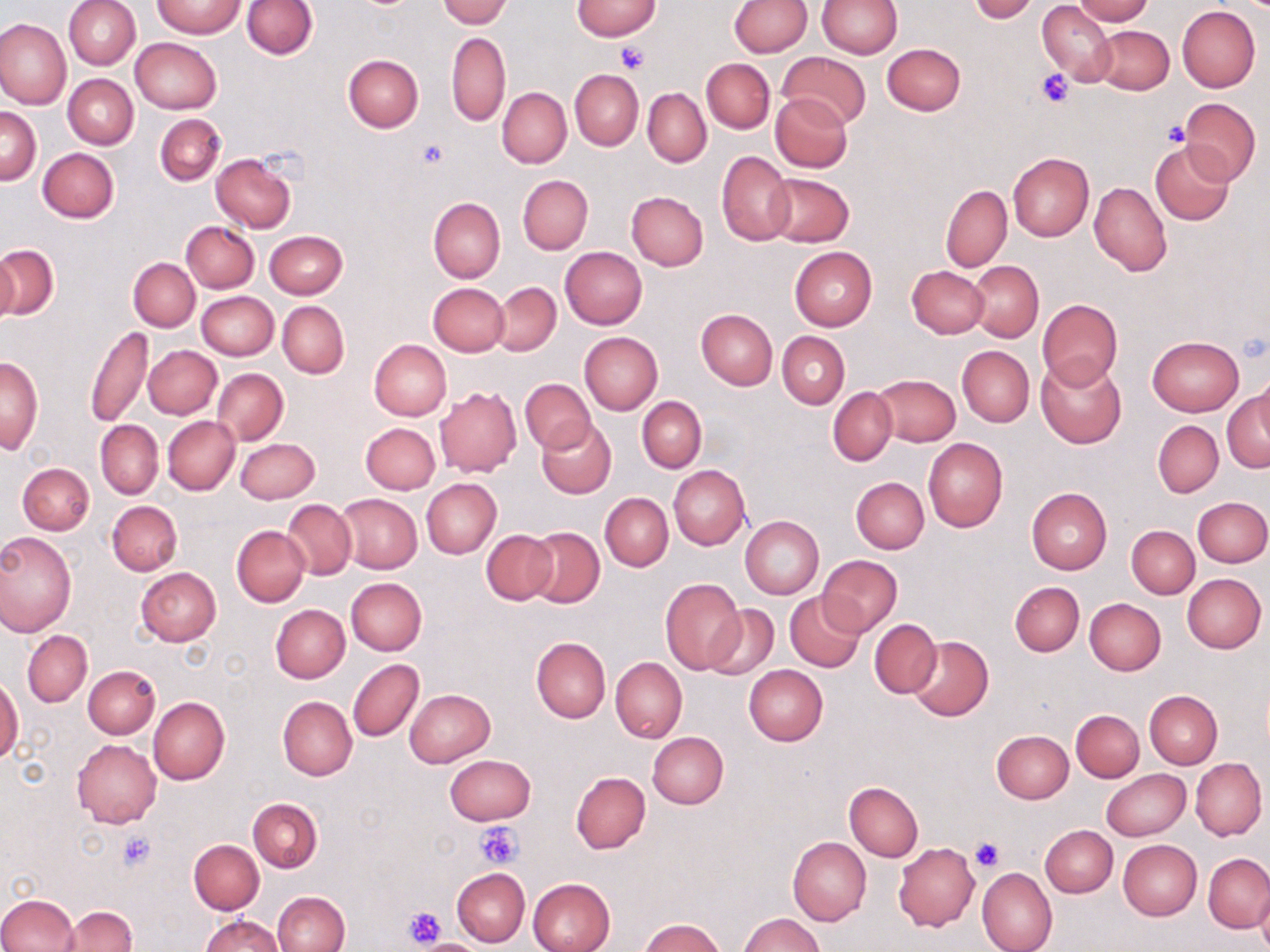

Summary:
  - Coordinate format: approximate bounding boxes as (x1, y1, x2, y2) in pixels
  - Uninfected red blood cell locations: (64, 0, 140, 69), (242, 0, 318, 59), (439, 0, 511, 27), (730, 0, 811, 56), (817, 0, 902, 58), (1072, 0, 1154, 25), (571, 1, 661, 39), (969, 1, 1039, 22), (152, 2, 246, 39), (1037, 3, 1117, 86), (1177, 6, 1260, 93), (0, 18, 71, 109), (1093, 25, 1173, 93), (446, 32, 511, 127), (131, 38, 223, 114), (882, 42, 965, 116), (776, 51, 872, 131), (343, 54, 423, 131), (701, 58, 774, 132), (570, 69, 643, 150), (64, 75, 138, 149), (497, 87, 571, 168), (643, 88, 711, 167), (770, 93, 852, 172), (1180, 98, 1261, 184), (1, 108, 42, 185), (155, 113, 226, 186), (1150, 142, 1236, 226), (38, 148, 119, 222), (717, 150, 795, 245), (1008, 152, 1093, 241), (211, 154, 297, 232), (765, 174, 854, 247), (518, 175, 593, 254), (1089, 181, 1171, 276), (941, 184, 1012, 272), (626, 191, 709, 271), (428, 198, 505, 284), (181, 222, 259, 294), (263, 230, 347, 299), (0, 245, 58, 320), (789, 246, 877, 331), (561, 247, 647, 330), (1, 248, 17, 326), (128, 258, 200, 331), (969, 261, 1043, 342), (907, 266, 989, 339), (491, 282, 560, 354), (428, 283, 508, 357), (196, 291, 279, 361), (1037, 299, 1123, 390), (277, 301, 349, 378), (696, 308, 777, 389), (85, 324, 154, 429), (777, 332, 850, 408), (580, 333, 662, 414), (1147, 336, 1243, 415), (369, 339, 451, 420), (144, 345, 222, 419), (957, 345, 1034, 426), (1, 356, 43, 454), (1036, 357, 1127, 449), (213, 369, 288, 445), (872, 374, 960, 446), (520, 378, 596, 453), (828, 386, 897, 465), (434, 387, 522, 477), (1222, 390, 1269, 473), (637, 396, 706, 472), (163, 416, 240, 495), (535, 419, 615, 497), (96, 420, 163, 499), (1153, 420, 1223, 498), (362, 422, 440, 494), (234, 438, 320, 504), (923, 438, 1007, 532), (18, 462, 95, 535), (668, 465, 750, 549), (851, 477, 929, 553), (421, 478, 502, 558), (1025, 487, 1111, 574), (600, 493, 672, 571), (335, 494, 421, 574), (1194, 496, 1270, 568), (107, 500, 182, 575), (284, 500, 356, 578), (740, 516, 823, 599), (1126, 525, 1201, 598), (231, 526, 310, 607), (526, 527, 604, 608), (482, 529, 557, 604), (0, 530, 76, 636), (817, 555, 902, 636), (135, 567, 220, 646), (1182, 574, 1266, 653), (346, 577, 426, 655), (660, 578, 746, 674), (1010, 582, 1084, 656), (784, 591, 866, 673), (1084, 598, 1166, 674), (703, 604, 778, 681), (271, 605, 350, 683), (870, 619, 941, 697), (23, 631, 92, 707), (906, 635, 994, 721), (531, 637, 611, 722), (611, 657, 686, 742), (348, 658, 423, 742), (743, 664, 828, 746), (83, 666, 159, 739), (0, 676, 23, 763), (405, 688, 495, 766), (1145, 691, 1221, 768), (277, 696, 356, 780), (149, 697, 229, 785), (1071, 710, 1144, 782), (992, 729, 1074, 803), (646, 731, 729, 809), (71, 739, 160, 828), (444, 754, 535, 825), (1191, 758, 1266, 840), (1102, 769, 1189, 841), (571, 771, 650, 854), (844, 782, 923, 860), (248, 798, 322, 872), (1041, 825, 1117, 898), (788, 837, 871, 925), (189, 840, 264, 914), (1118, 840, 1202, 921), (894, 844, 980, 931), (1204, 853, 1270, 932), (978, 867, 1057, 952), (452, 869, 529, 946), (528, 877, 616, 952), (1256, 888, 1270, 952), (272, 891, 350, 952), (0, 894, 78, 951), (58, 905, 136, 952), (738, 912, 825, 952), (202, 915, 283, 952), (640, 918, 724, 952), (415, 939, 482, 951)
  - Platelet locations: (614, 43, 650, 75), (1035, 69, 1074, 107), (1163, 120, 1191, 146), (415, 140, 449, 172), (474, 822, 524, 871), (118, 831, 156, 871), (969, 836, 1003, 872), (401, 905, 445, 947), (416, 936, 480, 950)
  - Slide-level diagnosis: no evidence of blood parasites
  - Stain: May-Grünwald-Giemsa
  - Preparation: thin blood smear
  - Field of view: one of a larger specimen
  - Modality: optical microscopy
  - Image size: 1270×952 pixels
  - Magnification: 1000x